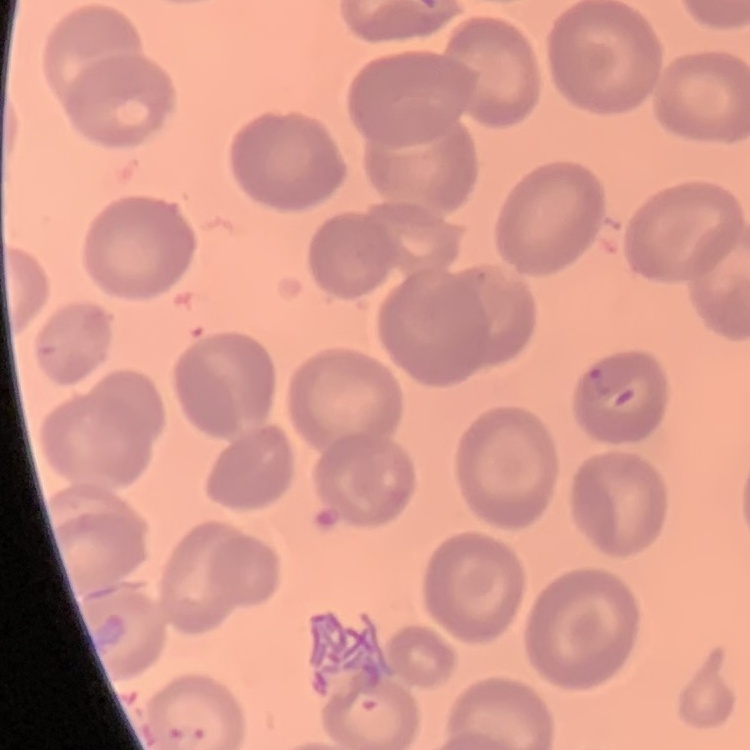 The erythrocytes show no rouleaux formation. One tile cut from a larger photomicrograph. Stained with either Field's or Giemsa. Thin blood film.